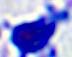 400x magnification. A leukocyte is seen. Photomicrograph.